Locate every uninfected red blood cell.
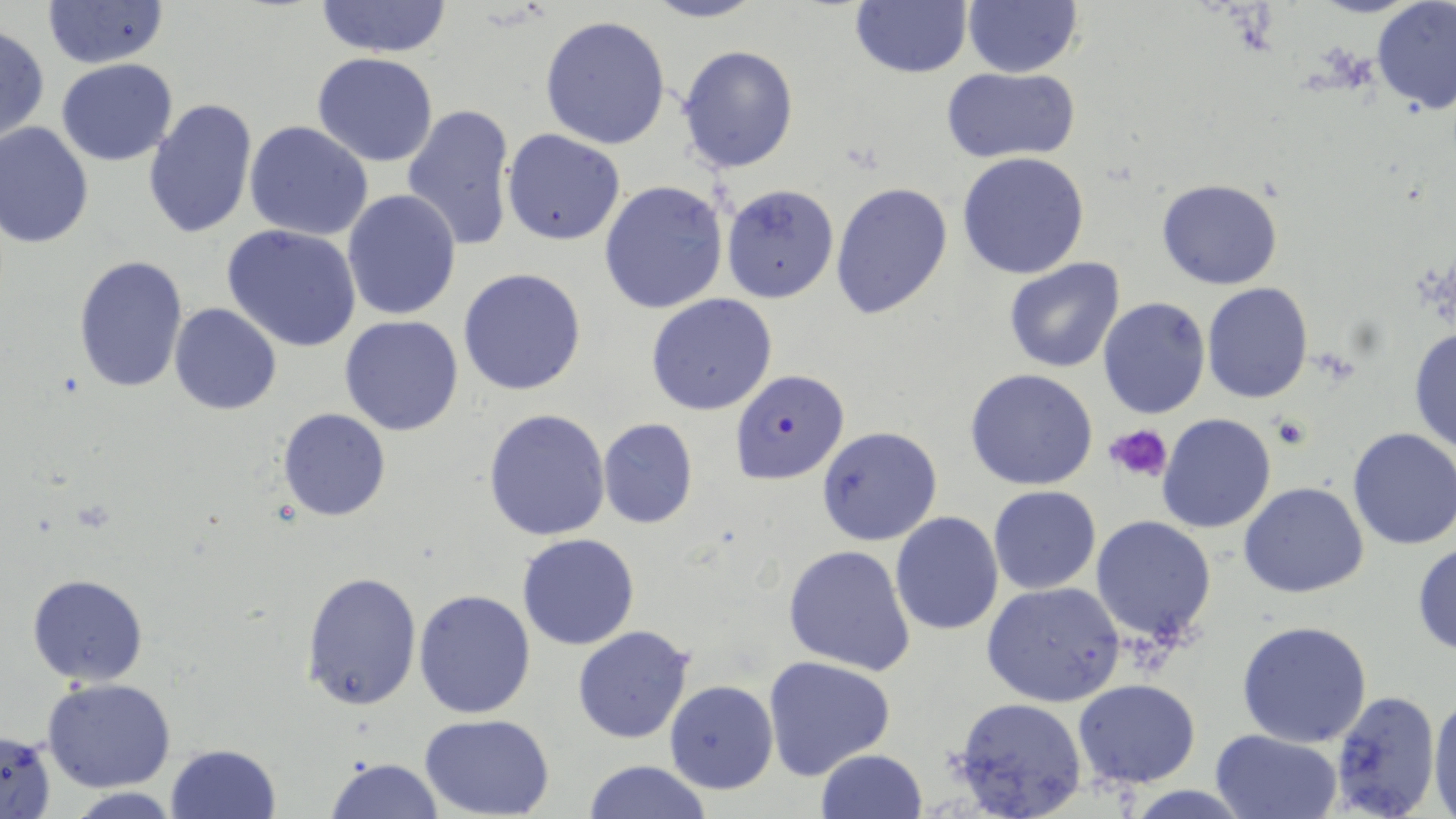

Approximate bounding boxes as [x1, y1, x2, y2] in pixels.
Uninfected red blood cells: [41, 0, 169, 68], [313, 0, 454, 57], [641, 0, 766, 23], [962, 0, 1083, 77], [849, 1, 973, 77], [1371, 2, 1455, 115], [538, 15, 671, 151], [0, 24, 49, 144], [678, 45, 799, 173], [313, 52, 439, 167], [55, 58, 178, 166], [940, 67, 1080, 162], [143, 98, 257, 239], [402, 103, 518, 255], [244, 121, 374, 241], [0, 122, 95, 249], [501, 129, 626, 246], [957, 152, 1091, 280], [1157, 178, 1285, 289], [599, 180, 729, 317], [829, 182, 954, 323], [720, 183, 839, 302], [342, 189, 462, 322], [222, 225, 363, 353], [73, 255, 190, 396], [1003, 257, 1126, 373], [458, 268, 586, 396], [1202, 282, 1314, 402], [646, 293, 778, 416], [1098, 297, 1211, 420], [170, 304, 282, 415], [339, 316, 465, 436], [1408, 325, 1456, 455], [966, 368, 1099, 491], [277, 408, 390, 522], [482, 408, 612, 542], [1156, 414, 1277, 534], [597, 418, 699, 529], [816, 425, 942, 546], [1345, 427, 1456, 550], [1239, 482, 1369, 599], [988, 486, 1101, 595], [889, 511, 1004, 635], [1090, 515, 1216, 649], [515, 533, 639, 651], [1412, 540, 1456, 657], [783, 544, 915, 674], [299, 569, 421, 711], [27, 573, 148, 685], [980, 582, 1125, 706], [413, 588, 537, 720], [1237, 621, 1372, 748], [572, 626, 697, 744], [764, 654, 896, 779], [41, 675, 176, 794], [1074, 678, 1201, 787], [664, 681, 777, 794], [1329, 689, 1442, 818], [1429, 692, 1456, 815], [950, 696, 1088, 819], [421, 715, 554, 819], [1210, 730, 1341, 817], [0, 732, 58, 818], [164, 742, 283, 819], [813, 749, 927, 819], [325, 756, 443, 818], [582, 760, 713, 818], [1119, 784, 1257, 817], [57, 789, 188, 818].

plasmodium_falciparum_infected_red_blood_cell_locations: 'approximate bounding boxes as [x1, y1, x2, y2] in pixels: [730, 370, 849, 486]'
slide_level_diagnosis: Plasmodium falciparum
magnification: 1000x
image_size: 1456×819 pixels
stain: May-Grünwald-Giemsa
platelet_locations: 'approximate bounding boxes as [x1, y1, x2, y2] in pixels: [1104, 423, 1175, 483]'
preparation: thin blood smear
modality: light microscopy
field_of_view: single